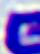
magnification = 400x
modality = micrograph
identification = white blood cell